Describe the morphology of the red blood cells.
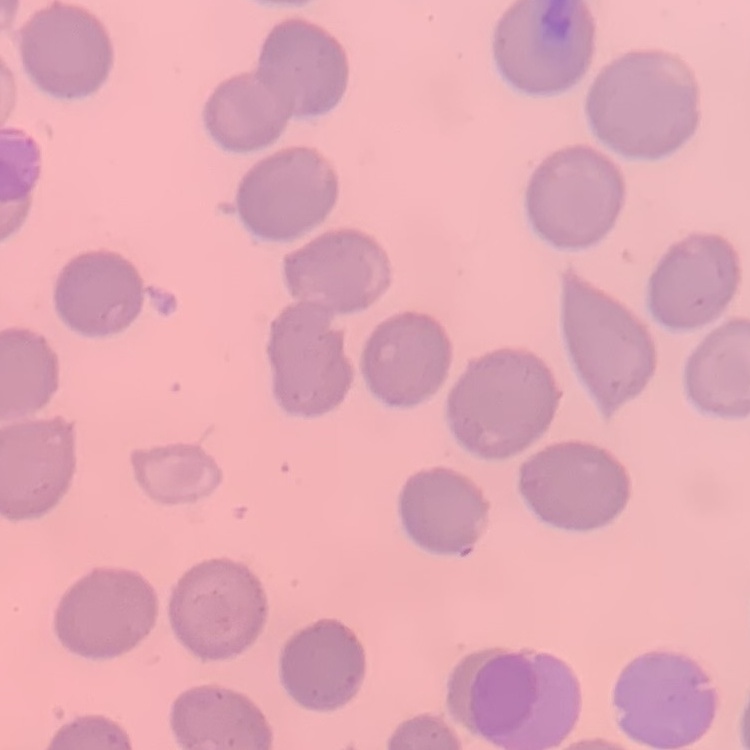

They show no rouleaux formation.

image type = one tile cut from a larger photomicrograph
stain = Field's or Giemsa
preparation = thin blood film